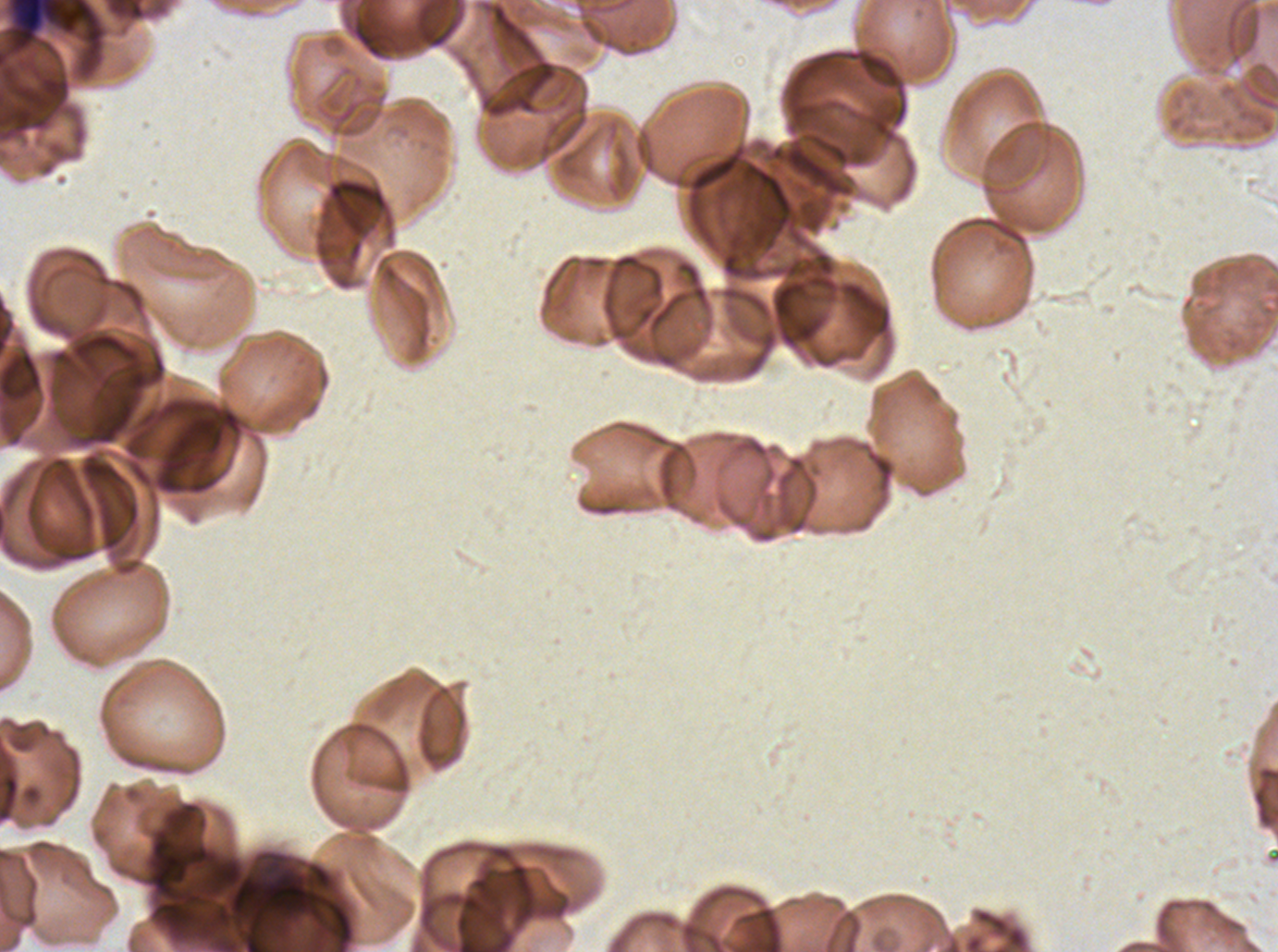

Approximate bounding boxes as {x1, y1, x2, y2} in pixels.
Summary:
  - Debris locations: {11, 0, 60, 42}
  - Preparation: thin blood smear
  - Image size: 1278×952 pixels
  - Specimen: P. falciparum from a patient in The Gambia, cultured ex vivo for 24 to 48 hours
  - Field of view: sub-image separated from a larger composite
  - Stain: Giemsa